Give the position of every leukocyte visible.
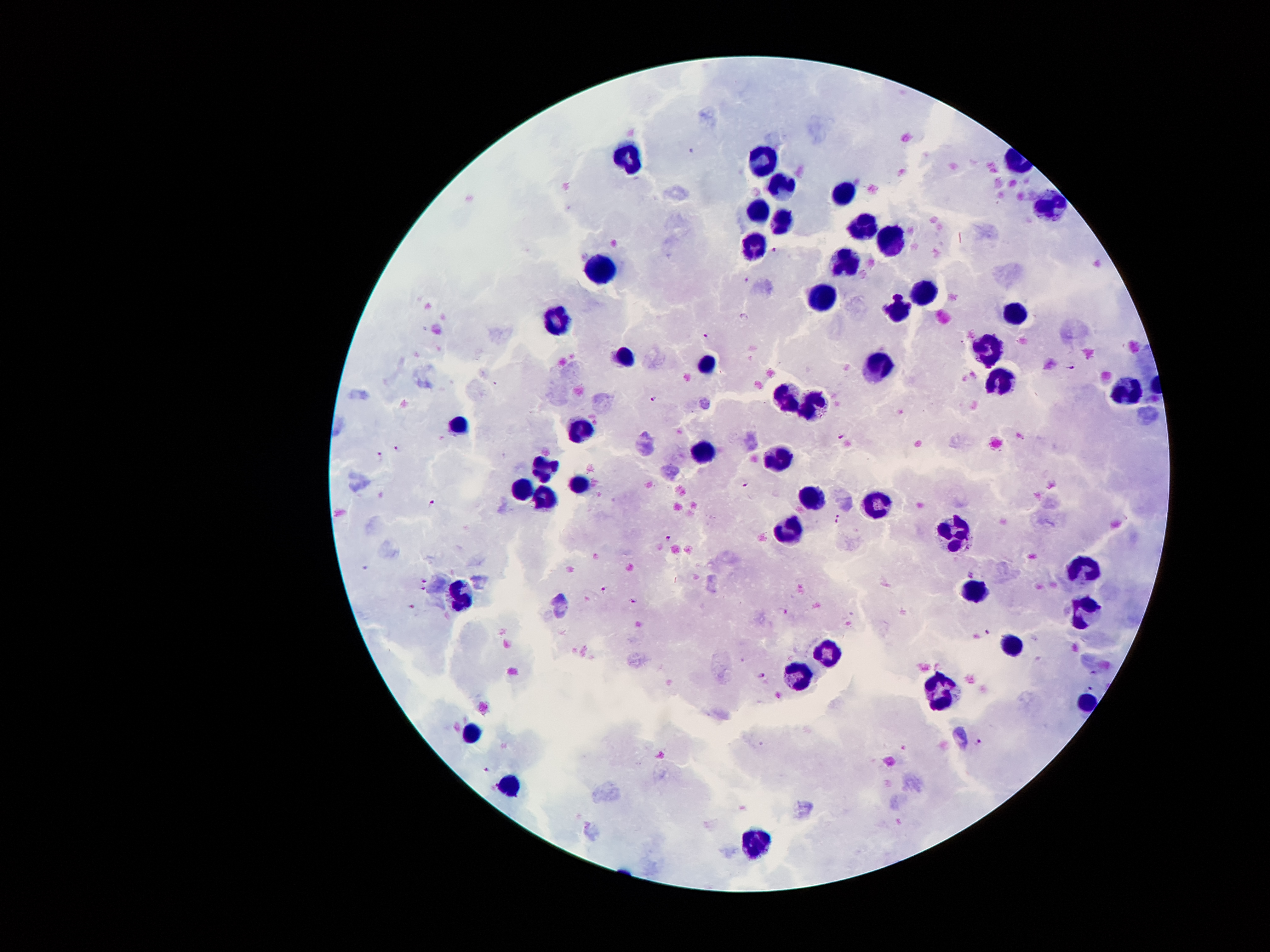
Approximate centers as (x, y) in pixels.
Leukocytes: (634, 155), (763, 164), (781, 190), (844, 193), (1052, 204), (759, 212), (780, 223), (864, 227), (890, 239), (753, 248), (845, 261), (603, 267), (924, 290), (825, 294), (902, 308), (1014, 313), (561, 321), (990, 346), (623, 356), (708, 363), (878, 365), (999, 385), (1123, 391), (789, 396), (812, 405), (580, 425), (461, 426), (706, 452), (781, 458), (546, 471), (575, 483), (522, 490), (545, 497), (810, 498), (879, 504), (955, 531), (791, 532), (1081, 568), (463, 593), (978, 593), (1085, 610), (1012, 648), (829, 654), (799, 675), (939, 688), (1085, 701), (469, 738), (507, 788), (752, 844).

Summary:
  - Plasmodium parasite locations: (693, 151), (775, 249), (747, 280), (743, 318), (706, 336), (1072, 368), (653, 398), (841, 435), (396, 448), (381, 457), (745, 484), (433, 503), (839, 518), (668, 538), (971, 575), (424, 580), (424, 588), (603, 588), (634, 600), (411, 606), (785, 610), (988, 632), (1094, 672), (762, 675), (1090, 687), (980, 741), (489, 768)
  - Field of view: one from this slide
  - Stain: Giemsa
  - Capture: smartphone through the microscope eyepiece
  - Patient malaria status: infected with Plasmodium falciparum
  - Magnification: 100x
  - Preparation: thick blood film
  - Image size: 1270×952 pixels